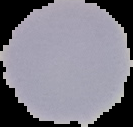 Image is 133×127 pixels. Segmented cell region on a black background. From a thin blood film. Malaria status: uninfected.